Look for parasitized red blood cells.
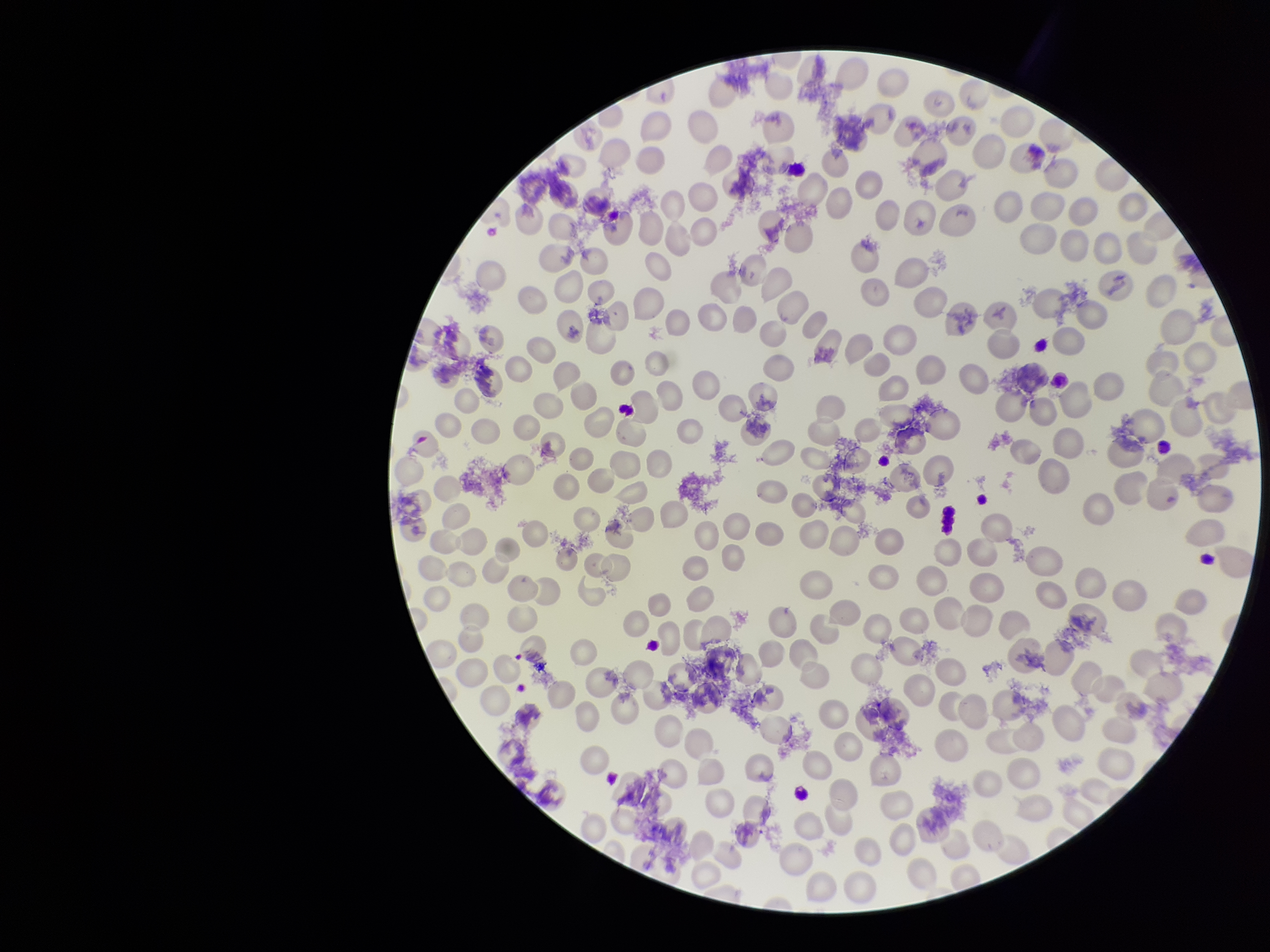
None identified.

Summary:
  - Red blood cell count: 211
  - Patient malaria status: negative
  - Preparation: thin smear
  - Image size: 1270×952 pixels
  - Parasitized red blood cell count: 0
  - Capture: smartphone photograph through the microscope eyepiece
  - Stain: Giemsa
  - Field of view: one from this slide